Locate every Plasmodium malariae-infected red blood cell.
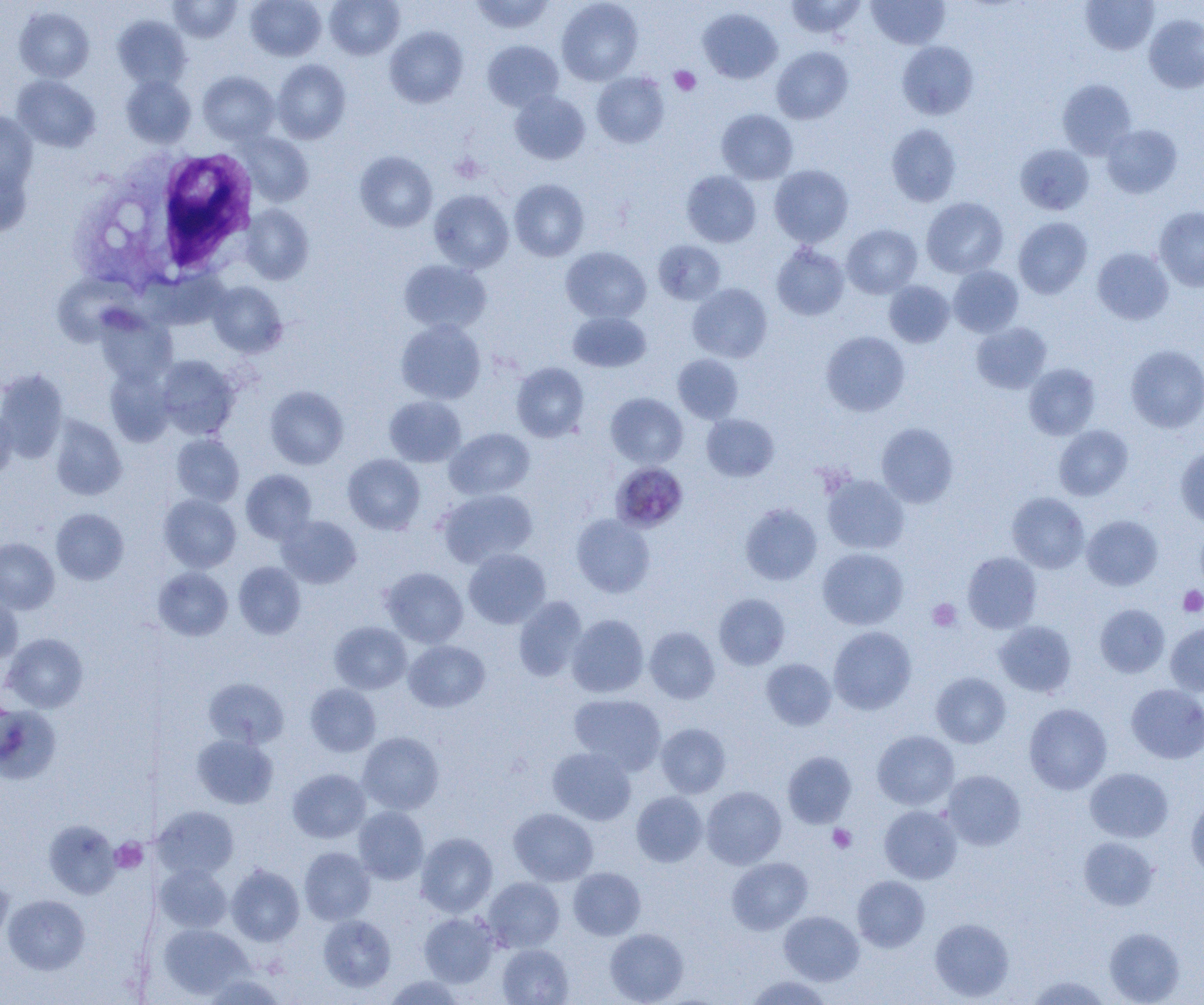

Approximate bounding boxes as named x1/y1/x2/y2 corners in pixels.
Plasmodium malariae-infected red blood cells: (x1=610, y1=462, x2=688, y2=533).

slide-level diagnosis = Plasmodium malariae
uninfected red blood cell locations = approximate bounding boxes as named x1/y1/x2/y2 corners in pixels: (x1=167, y1=0, x2=243, y2=43), (x1=245, y1=0, x2=326, y2=61), (x1=324, y1=0, x2=404, y2=59), (x1=469, y1=0, x2=555, y2=34), (x1=557, y1=0, x2=643, y2=85), (x1=784, y1=0, x2=867, y2=39), (x1=1080, y1=0, x2=1159, y2=55), (x1=867, y1=1, x2=949, y2=49), (x1=14, y1=7, x2=94, y2=82), (x1=698, y1=7, x2=782, y2=84), (x1=1144, y1=14, x2=1204, y2=93), (x1=113, y1=15, x2=192, y2=91), (x1=384, y1=26, x2=468, y2=108), (x1=483, y1=40, x2=563, y2=111), (x1=897, y1=41, x2=978, y2=119), (x1=772, y1=47, x2=853, y2=124), (x1=272, y1=59, x2=351, y2=143), (x1=198, y1=71, x2=279, y2=145), (x1=592, y1=72, x2=669, y2=147), (x1=12, y1=75, x2=100, y2=152), (x1=121, y1=75, x2=196, y2=148), (x1=1057, y1=79, x2=1137, y2=158), (x1=510, y1=91, x2=590, y2=164), (x1=716, y1=109, x2=798, y2=184), (x1=0, y1=112, x2=38, y2=193), (x1=886, y1=123, x2=962, y2=207), (x1=1101, y1=124, x2=1182, y2=198), (x1=239, y1=132, x2=314, y2=206), (x1=1015, y1=144, x2=1094, y2=215), (x1=355, y1=151, x2=437, y2=232), (x1=0, y1=161, x2=32, y2=237), (x1=769, y1=165, x2=854, y2=247), (x1=681, y1=170, x2=761, y2=247), (x1=509, y1=179, x2=590, y2=261), (x1=429, y1=190, x2=514, y2=273), (x1=921, y1=197, x2=1008, y2=278), (x1=243, y1=204, x2=314, y2=285), (x1=1154, y1=207, x2=1204, y2=291), (x1=1013, y1=217, x2=1093, y2=299), (x1=841, y1=225, x2=922, y2=298), (x1=653, y1=240, x2=726, y2=305), (x1=771, y1=244, x2=849, y2=320), (x1=560, y1=247, x2=651, y2=323), (x1=1092, y1=247, x2=1173, y2=325), (x1=398, y1=259, x2=491, y2=334), (x1=948, y1=265, x2=1024, y2=337), (x1=884, y1=280, x2=954, y2=347), (x1=207, y1=281, x2=287, y2=357), (x1=687, y1=284, x2=772, y2=362), (x1=567, y1=311, x2=651, y2=372), (x1=96, y1=312, x2=176, y2=386), (x1=396, y1=319, x2=486, y2=404), (x1=971, y1=322, x2=1052, y2=393), (x1=821, y1=331, x2=910, y2=416), (x1=1125, y1=344, x2=1204, y2=433), (x1=672, y1=353, x2=743, y2=423), (x1=155, y1=355, x2=241, y2=439), (x1=512, y1=362, x2=589, y2=441), (x1=1024, y1=363, x2=1101, y2=440), (x1=105, y1=366, x2=176, y2=446), (x1=0, y1=369, x2=68, y2=463), (x1=265, y1=386, x2=349, y2=469), (x1=606, y1=393, x2=688, y2=469), (x1=384, y1=395, x2=466, y2=467), (x1=0, y1=407, x2=17, y2=479), (x1=702, y1=414, x2=779, y2=481), (x1=49, y1=416, x2=127, y2=500), (x1=876, y1=423, x2=958, y2=507), (x1=1054, y1=425, x2=1133, y2=500), (x1=445, y1=428, x2=535, y2=500), (x1=171, y1=433, x2=244, y2=506), (x1=1175, y1=446, x2=1204, y2=527), (x1=342, y1=454, x2=425, y2=534), (x1=241, y1=469, x2=317, y2=544), (x1=822, y1=474, x2=909, y2=554), (x1=437, y1=488, x2=537, y2=568), (x1=1007, y1=492, x2=1089, y2=573), (x1=159, y1=494, x2=241, y2=572), (x1=739, y1=503, x2=822, y2=586), (x1=51, y1=508, x2=128, y2=584), (x1=571, y1=513, x2=655, y2=598), (x1=276, y1=515, x2=362, y2=589), (x1=1082, y1=515, x2=1163, y2=590), (x1=1195, y1=524, x2=1204, y2=596), (x1=0, y1=538, x2=59, y2=614), (x1=817, y1=547, x2=908, y2=630), (x1=464, y1=548, x2=551, y2=628), (x1=962, y1=551, x2=1042, y2=633), (x1=234, y1=561, x2=305, y2=639), (x1=153, y1=567, x2=233, y2=641), (x1=380, y1=567, x2=469, y2=648), (x1=0, y1=592, x2=23, y2=664), (x1=714, y1=593, x2=790, y2=670), (x1=513, y1=596, x2=587, y2=682), (x1=1095, y1=604, x2=1170, y2=677), (x1=567, y1=614, x2=649, y2=697), (x1=329, y1=621, x2=412, y2=694), (x1=994, y1=621, x2=1076, y2=697), (x1=1165, y1=621, x2=1204, y2=696), (x1=828, y1=626, x2=916, y2=714), (x1=645, y1=627, x2=720, y2=703), (x1=2, y1=633, x2=88, y2=713), (x1=404, y1=640, x2=490, y2=712), (x1=761, y1=658, x2=836, y2=730), (x1=931, y1=672, x2=1011, y2=748), (x1=204, y1=678, x2=288, y2=748), (x1=305, y1=683, x2=381, y2=757), (x1=1126, y1=683, x2=1204, y2=763), (x1=569, y1=694, x2=666, y2=774), (x1=1024, y1=703, x2=1112, y2=794), (x1=0, y1=705, x2=62, y2=784), (x1=656, y1=723, x2=731, y2=798), (x1=872, y1=730, x2=959, y2=810), (x1=357, y1=732, x2=444, y2=814), (x1=192, y1=734, x2=278, y2=808), (x1=547, y1=747, x2=636, y2=825), (x1=783, y1=751, x2=856, y2=827), (x1=1085, y1=768, x2=1173, y2=843), (x1=287, y1=769, x2=370, y2=843), (x1=942, y1=770, x2=1026, y2=850), (x1=701, y1=786, x2=786, y2=869), (x1=631, y1=791, x2=708, y2=867), (x1=1186, y1=797, x2=1204, y2=879), (x1=879, y1=805, x2=962, y2=884), (x1=152, y1=806, x2=239, y2=880), (x1=354, y1=806, x2=429, y2=884), (x1=508, y1=808, x2=598, y2=885), (x1=44, y1=820, x2=120, y2=899), (x1=416, y1=832, x2=498, y2=917), (x1=1078, y1=836, x2=1159, y2=911), (x1=299, y1=847, x2=376, y2=925), (x1=727, y1=857, x2=812, y2=934), (x1=155, y1=863, x2=232, y2=932), (x1=226, y1=864, x2=304, y2=946), (x1=568, y1=867, x2=645, y2=939), (x1=852, y1=875, x2=929, y2=952), (x1=483, y1=877, x2=564, y2=952), (x1=0, y1=878, x2=13, y2=949), (x1=2, y1=894, x2=90, y2=975), (x1=779, y1=911, x2=864, y2=985), (x1=419, y1=912, x2=500, y2=988), (x1=318, y1=914, x2=396, y2=992), (x1=930, y1=918, x2=1014, y2=1001), (x1=157, y1=922, x2=253, y2=999), (x1=1104, y1=927, x2=1185, y2=1004), (x1=605, y1=928, x2=689, y2=1004), (x1=498, y1=944, x2=573, y2=1004), (x1=203, y1=973, x2=285, y2=1005), (x1=383, y1=975, x2=465, y2=1004), (x1=743, y1=975, x2=835, y2=1005), (x1=1026, y1=975, x2=1112, y2=1005)
preparation = thin blood film
field of view = one of a larger specimen
magnification = 1000x
white blood cell locations = approximate bounding boxes as named x1/y1/x2/y2 corners in pixels: (x1=78, y1=144, x2=261, y2=293)
platelet locations = approximate bounding boxes as named x1/y1/x2/y2 corners in pixels: (x1=670, y1=66, x2=700, y2=95), (x1=450, y1=153, x2=485, y2=183), (x1=1178, y1=586, x2=1204, y2=617), (x1=927, y1=598, x2=962, y2=632), (x1=828, y1=824, x2=856, y2=853), (x1=110, y1=838, x2=148, y2=873)
image size = 1204×1005 pixels
modality = optical microscopy